State which cell type is depicted.
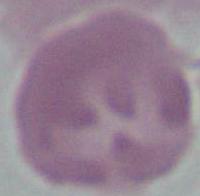

This is an erythrocyte.

modality = micrograph
magnification = 1000x